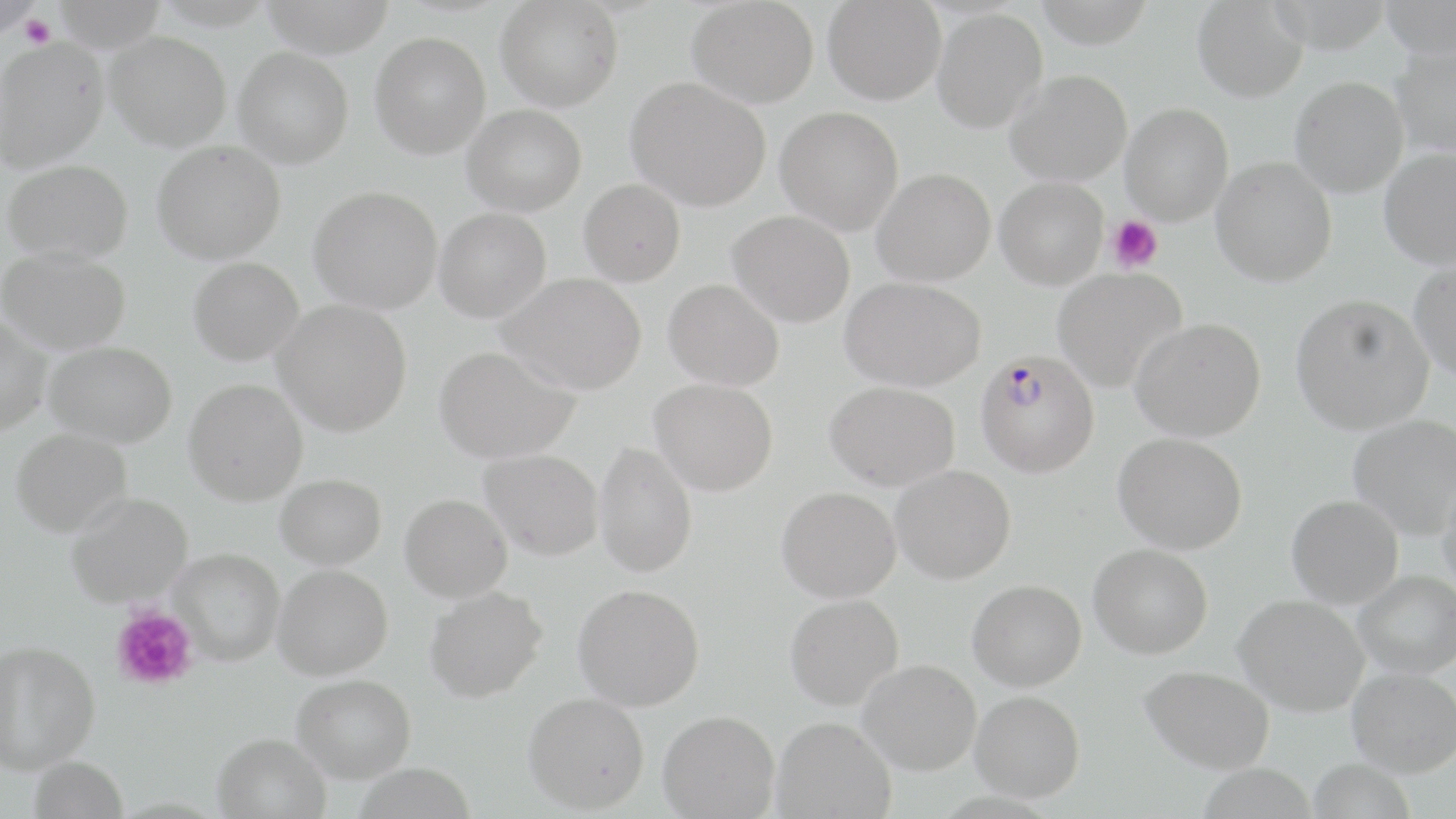
Summary:
  - Coordinate format: approximate bounding boxes as (x1, y1, x2, y2) in pixels
  - Plasmodium falciparum-infected red blood cell locations: (975, 350, 1099, 477)
  - Uninfected red blood cell locations: (0, 0, 38, 39), (51, 0, 168, 51), (259, 0, 396, 56), (495, 0, 622, 112), (687, 0, 819, 107), (823, 0, 945, 105), (1379, 0, 1456, 58), (1192, 1, 1308, 102), (932, 9, 1047, 133), (106, 31, 231, 150), (370, 32, 490, 158), (0, 36, 107, 171), (1391, 42, 1456, 157), (234, 47, 353, 168), (1005, 69, 1132, 186), (626, 76, 771, 211), (1290, 76, 1408, 197), (1120, 103, 1233, 225), (462, 105, 587, 215), (775, 106, 903, 234), (153, 140, 286, 264), (1379, 147, 1455, 270), (1211, 157, 1337, 286), (2, 159, 133, 262), (873, 169, 995, 286), (995, 177, 1108, 289), (578, 179, 685, 286), (309, 185, 442, 313), (434, 208, 551, 322), (728, 211, 855, 327), (0, 247, 132, 354), (188, 257, 304, 365), (1409, 261, 1456, 380), (1052, 267, 1187, 392), (498, 272, 647, 394), (840, 276, 986, 391), (663, 279, 784, 390), (1291, 293, 1434, 434), (273, 299, 412, 435), (0, 316, 51, 436), (1130, 317, 1267, 441), (43, 341, 177, 447), (434, 345, 579, 463), (184, 378, 309, 505), (650, 379, 778, 496), (825, 382, 960, 491), (1348, 414, 1456, 539), (10, 427, 132, 537), (1113, 432, 1247, 554), (594, 441, 697, 578), (479, 449, 603, 560), (890, 465, 1016, 584), (275, 473, 387, 569), (1437, 478, 1456, 599), (777, 486, 901, 603), (66, 492, 192, 607), (400, 494, 512, 602), (1286, 494, 1404, 608), (1089, 543, 1212, 659), (169, 548, 285, 665), (273, 565, 393, 680), (1355, 571, 1456, 678), (967, 579, 1087, 691), (573, 583, 705, 711), (424, 585, 547, 702), (785, 594, 903, 710), (1234, 594, 1369, 716), (0, 640, 100, 772), (858, 659, 981, 775), (1139, 665, 1275, 773), (1347, 667, 1456, 777), (293, 674, 416, 783), (971, 690, 1085, 802), (523, 692, 650, 813), (658, 710, 780, 818), (772, 716, 896, 818), (212, 732, 331, 819), (28, 756, 128, 819)
  - Platelet locations: (20, 15, 56, 48), (1108, 215, 1163, 273), (112, 606, 197, 690)
  - Slide-level diagnosis: Plasmodium falciparum
  - Stain: May-Grünwald-Giemsa
  - Modality: light microscopy
  - Preparation: thin blood smear
  - Field of view: single
  - Image size: 1456×819 pixels
  - Magnification: 1000x